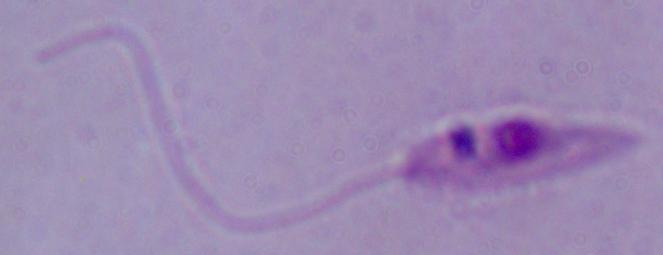

Summary:
  - Identification: Leishmania
  - Modality: photomicrograph
  - Magnification: 1000x